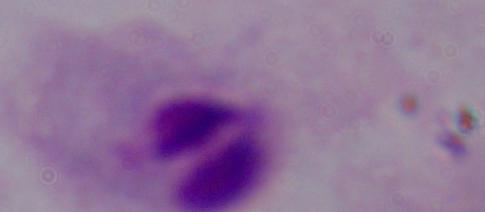

magnification = 1000x
identification = trichomonad
modality = micrograph